Locate every Plasmodium parasite.
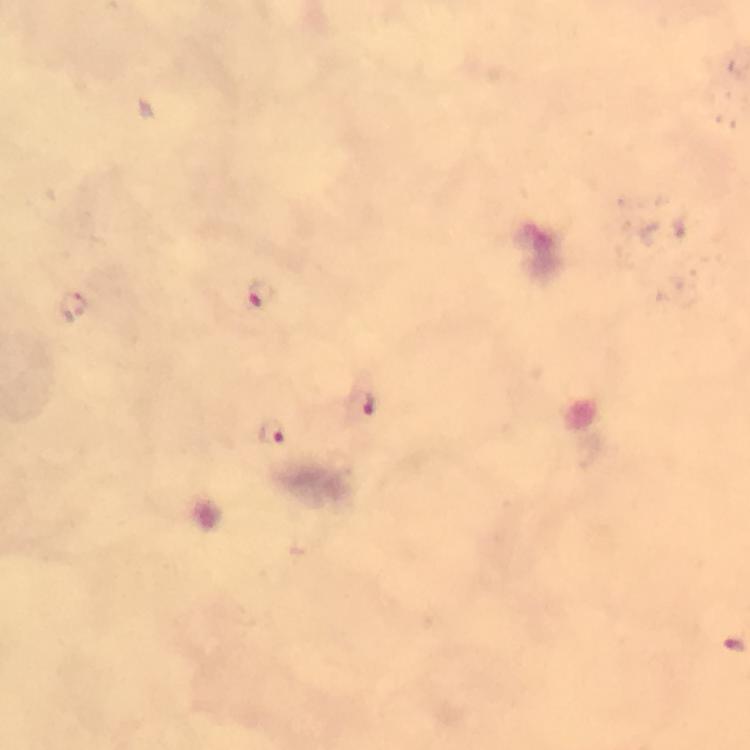

Approximate centers as [x, y] in pixels.
Plasmodium parasites: [261, 290], [371, 404], [271, 434].

{
  "preparation": "thick smear",
  "magnification": "100x",
  "image_size": "750×750 pixels",
  "cropped_from": "a single field of view",
  "stain": "Giemsa",
  "capture": "smartphone photograph through a microscope",
  "immersion_oil": "applied",
  "context": "from a diagnostic examination for malaria"
}